State the blood parasite species.
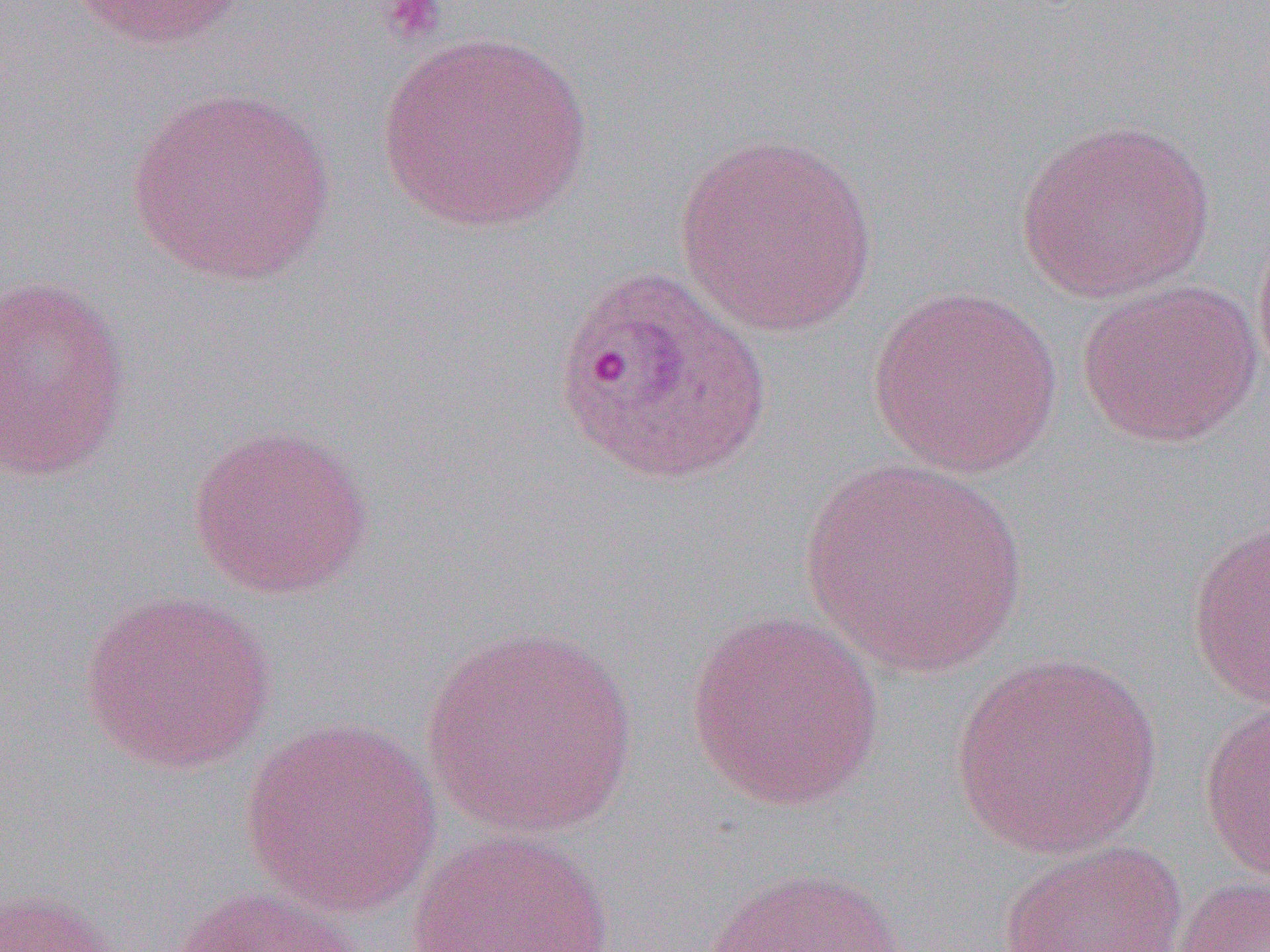

Plasmodium ovale.

Summary:
  - Coordinate format: approximate bounding boxes as (x1, y1, x2, y2) in pixels
  - Uninfected red blood cell locations: (64, 0, 249, 50), (374, 31, 595, 233), (124, 86, 337, 286), (1016, 118, 1218, 304), (672, 131, 879, 339), (1252, 208, 1270, 395), (0, 274, 133, 483), (1075, 277, 1263, 448), (867, 285, 1065, 478), (186, 424, 375, 599), (801, 458, 1030, 680), (1186, 518, 1270, 711), (79, 588, 276, 775), (683, 610, 886, 811), (420, 622, 642, 843), (949, 651, 1164, 860), (1199, 701, 1269, 883), (239, 716, 444, 919), (405, 830, 615, 952), (997, 839, 1188, 951), (699, 863, 912, 952), (1173, 874, 1270, 952), (161, 884, 363, 952), (0, 887, 128, 952)
  - Plasmodium ovale-infected red blood cell locations: (551, 264, 772, 487)
  - Platelet locations: (381, 0, 448, 45)
  - Preparation: thin blood film
  - Field of view: one of a larger specimen
  - Modality: optical microscopy
  - Magnification: 1000x
  - Image size: 1270×952 pixels